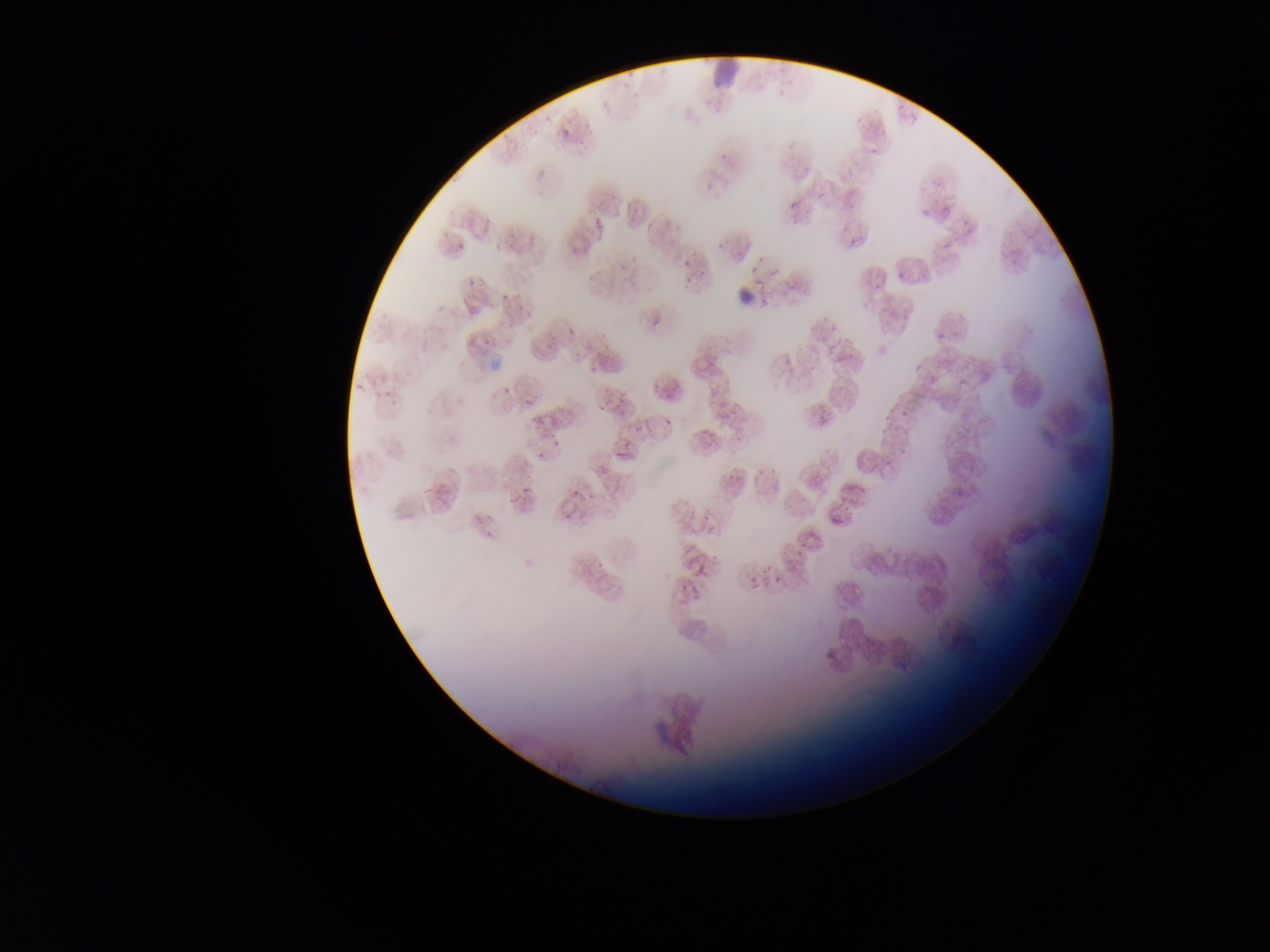

Approximate bounding boxes as [left, top, right, bottom] in pixels.
Summary:
  - Malaria parasite locations: [557, 122, 576, 137], [716, 142, 729, 169], [863, 143, 879, 159], [702, 163, 733, 189], [783, 191, 809, 217], [619, 197, 637, 212], [844, 198, 862, 209], [955, 212, 976, 227], [591, 218, 604, 231], [667, 222, 684, 240], [846, 232, 866, 247], [711, 235, 738, 250], [495, 236, 512, 248], [455, 238, 471, 252], [679, 254, 694, 269], [615, 258, 635, 274], [747, 260, 769, 270], [463, 267, 486, 287], [771, 268, 782, 280], [893, 268, 908, 285], [684, 274, 702, 287], [751, 277, 773, 291], [499, 290, 513, 306], [458, 294, 474, 312], [644, 312, 662, 334], [819, 316, 836, 334], [569, 326, 576, 334], [933, 327, 949, 348], [465, 337, 485, 352], [543, 337, 560, 350], [483, 339, 501, 350], [569, 347, 586, 362], [810, 356, 823, 375], [910, 360, 928, 375], [586, 364, 600, 375], [503, 384, 512, 395], [614, 384, 630, 406], [376, 388, 398, 402], [523, 396, 540, 413], [595, 401, 612, 412], [389, 403, 402, 413], [812, 404, 830, 424], [897, 409, 913, 420], [882, 412, 897, 430], [658, 419, 675, 427], [529, 423, 539, 427], [553, 438, 563, 448], [892, 440, 906, 458], [612, 449, 625, 459], [536, 451, 540, 459], [755, 465, 780, 491], [727, 467, 741, 486], [949, 480, 967, 500], [520, 481, 529, 493], [839, 487, 858, 505], [569, 490, 585, 502], [827, 509, 848, 531], [561, 510, 571, 519], [479, 523, 506, 544], [789, 530, 812, 561], [592, 557, 607, 573], [691, 558, 718, 577], [771, 561, 789, 587], [751, 568, 766, 590], [677, 581, 695, 605]
  - Preparation: thin blood film
  - Image size: 1270×952 pixels
  - Country: Ghana
  - Capture: mobile-phone photograph through a microscope
  - Field of view: single